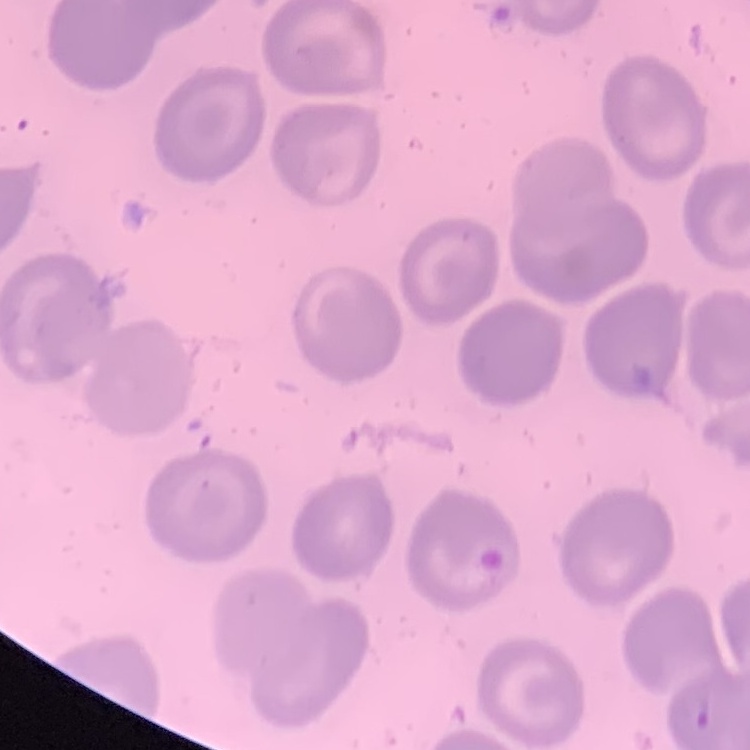
{
  "red_blood_cell_morphology": "no rouleaux formation",
  "image_type": "one tile cut from a larger photomicrograph",
  "preparation": "thin blood film",
  "stain": "Field's or Giemsa"
}